Report the malaria status of this cell.
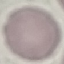
Uninfected.

image_type: automatically extracted cell patch, resized to 64 × 64 pixels
stain: Giemsa
capture: smartphone through the microscope eyepiece
preparation: thin blood smear